Give the extent of all Plasmodium malariae-infected red blood cells.
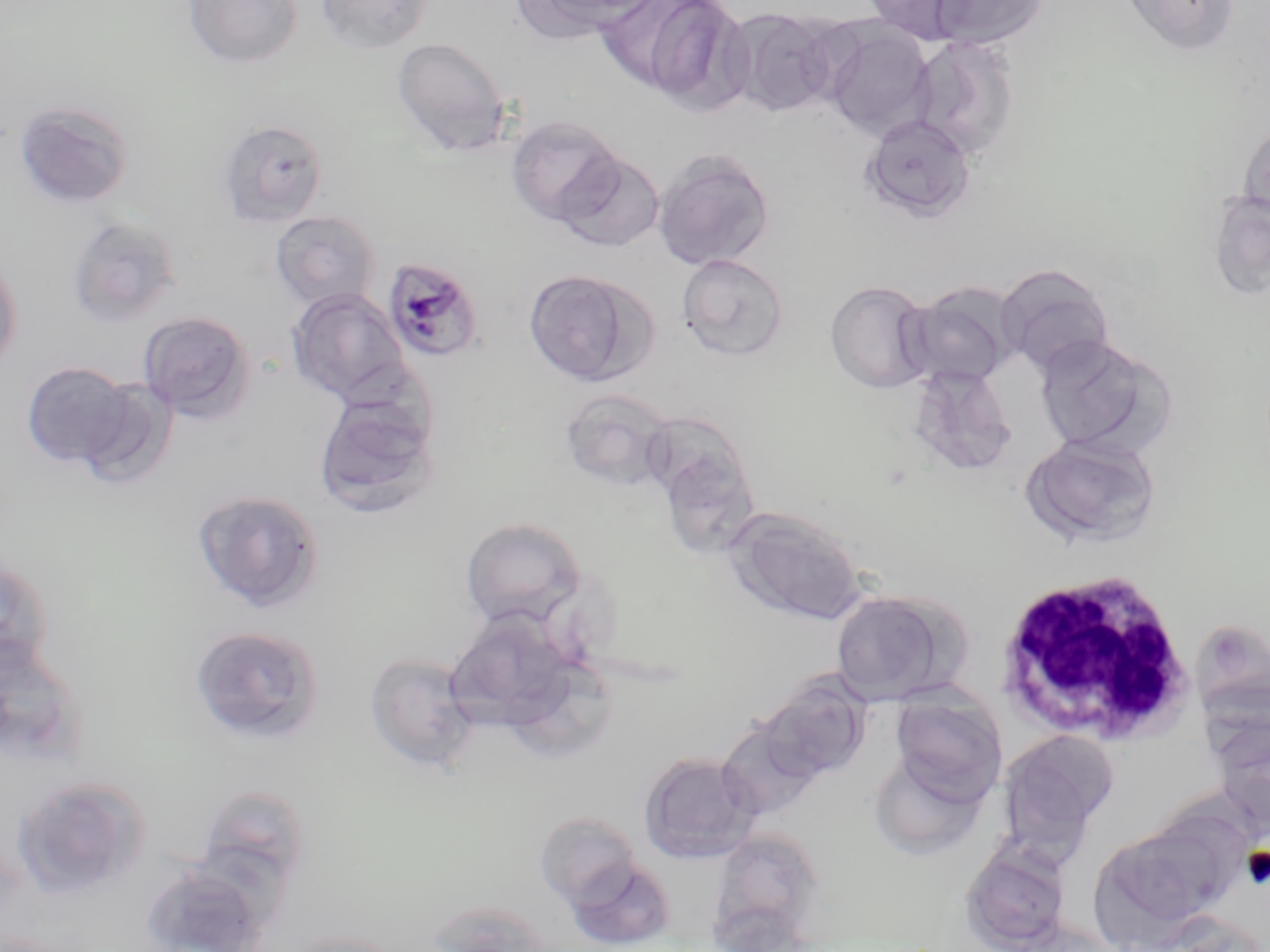
Approximate bounding boxes as [x1, y1, x2, y2] in pixels.
Plasmodium malariae-infected red blood cells: [382, 257, 484, 364].

slide-level diagnosis = Plasmodium malariae
magnification = 1000x
uninfected red blood cell locations = approximate bounding boxes as [x1, y1, x2, y2] in pixels: [183, 0, 302, 69], [314, 0, 431, 54], [515, 0, 658, 41], [604, 0, 752, 109], [860, 0, 977, 44], [928, 0, 1049, 51], [1120, 0, 1238, 56], [723, 7, 840, 117], [821, 22, 935, 138], [909, 34, 1020, 160], [392, 37, 511, 156], [13, 99, 134, 209], [860, 113, 977, 223], [506, 115, 624, 226], [217, 119, 329, 227], [1237, 121, 1270, 226], [653, 148, 775, 272], [554, 149, 666, 251], [1207, 190, 1270, 301], [270, 210, 382, 311], [66, 215, 183, 329], [0, 250, 23, 376], [676, 254, 789, 361], [996, 265, 1114, 376], [522, 268, 653, 386], [825, 280, 935, 394], [901, 282, 1022, 390], [286, 287, 411, 407], [138, 310, 256, 424], [1033, 334, 1175, 458], [20, 361, 134, 468], [907, 364, 1019, 477], [74, 377, 180, 490], [560, 388, 677, 493], [314, 390, 441, 519], [640, 418, 755, 516], [1020, 433, 1163, 549], [666, 454, 766, 559], [192, 489, 325, 613], [726, 508, 867, 625], [460, 516, 588, 629], [0, 552, 54, 678], [828, 589, 964, 705], [444, 607, 581, 739], [1190, 618, 1270, 719], [189, 625, 324, 746], [365, 652, 481, 773], [757, 674, 872, 784], [889, 691, 1007, 804], [1209, 716, 1270, 835], [716, 718, 824, 821], [997, 729, 1119, 855], [868, 750, 989, 860], [638, 751, 761, 864], [9, 773, 151, 901], [196, 783, 313, 892], [1135, 802, 1253, 915], [534, 811, 642, 909], [1088, 826, 1225, 948], [710, 829, 825, 944], [959, 840, 1072, 952], [564, 856, 677, 950], [141, 861, 272, 952], [428, 901, 556, 951], [281, 930, 410, 952]
field of view = single
image size = 1270×952 pixels
stain = May-Grünwald-Giemsa
modality = optical microscopy
white blood cell locations = approximate bounding boxes as [x1, y1, x2, y2] in pixels: [998, 569, 1197, 746]
preparation = thin blood film